Classify this cell by malaria status.
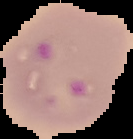
Parasitized.

{
  "image_size": "133×139 pixels",
  "image_type": "segmented cell region with the area outside set to black",
  "preparation": "thin blood smear"
}